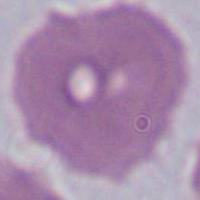 Captured at 1000x magnification. Photomicrograph. A red blood cell is shown.